Describe the morphology of the red blood cells.
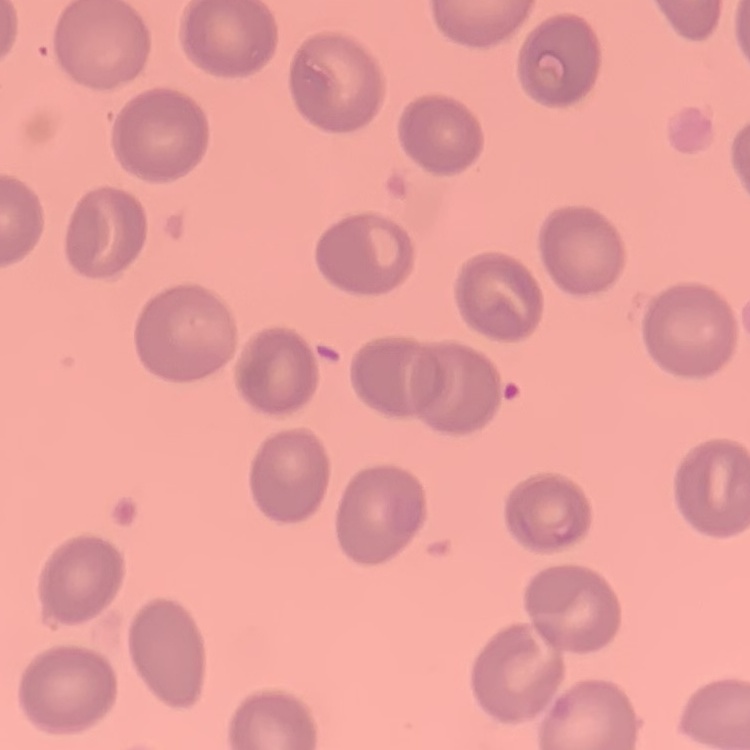
No rouleaux formation.

{
  "preparation": "thin blood smear",
  "stain": "Field's or Giemsa",
  "image_type": "one tile cut from a larger photomicrograph"
}